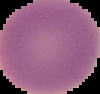
preparation = thin blood film
image size = 100×94 pixels
result = no Plasmodium parasites detected
image type = segmented cell region with the area outside set to black